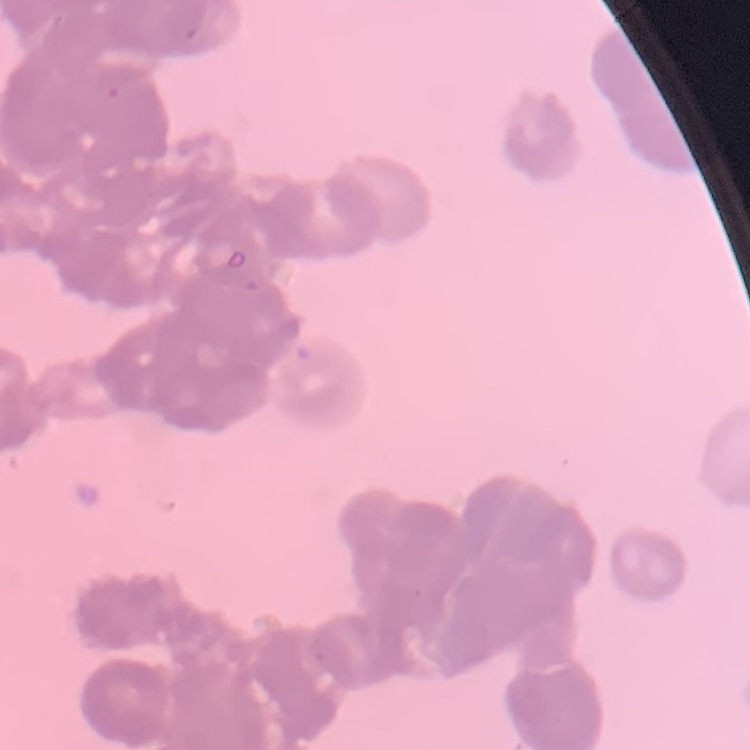
Summary:
  - Erythrocyte morphology: rouleaux formation
  - Stain: Field's or Giemsa
  - Image type: square crop of a larger photomicrograph
  - Preparation: thin peripheral smear